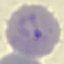
Result: malaria parasites identified. Giemsa-stained preparation. Photographed with a smartphone camera at the microscope eyepiece. Thin smear of blood. Automatically extracted cell patch, resized to 64 × 64 pixels.